Report the malaria status of this cell.
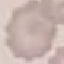
Uninfected.

Automatically extracted cell patch, resized to 64 × 64 pixels. Giemsa-stained preparation. Acquired by smartphone through the microscope eyepiece. Thin smear of blood.